Assess this cell for malaria.
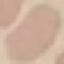
Uninfected.

Summary:
  - Preparation: thin blood smear
  - Capture: smartphone through the microscope eyepiece
  - Stain: Giemsa
  - Image type: cell patch, automatically extracted from a larger field of view and resized to 64 × 64 pixels